Identify the parasite.
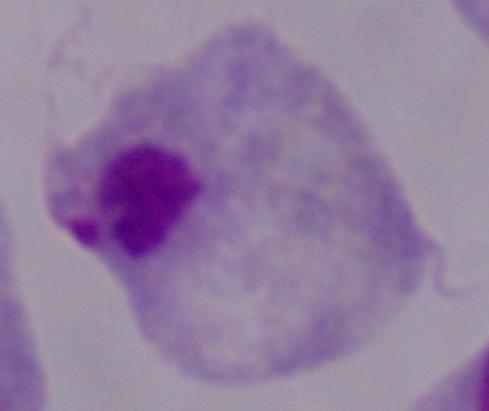

This is a trichomonad.

magnification = 1000x
modality = photomicrograph